Locate platelets.
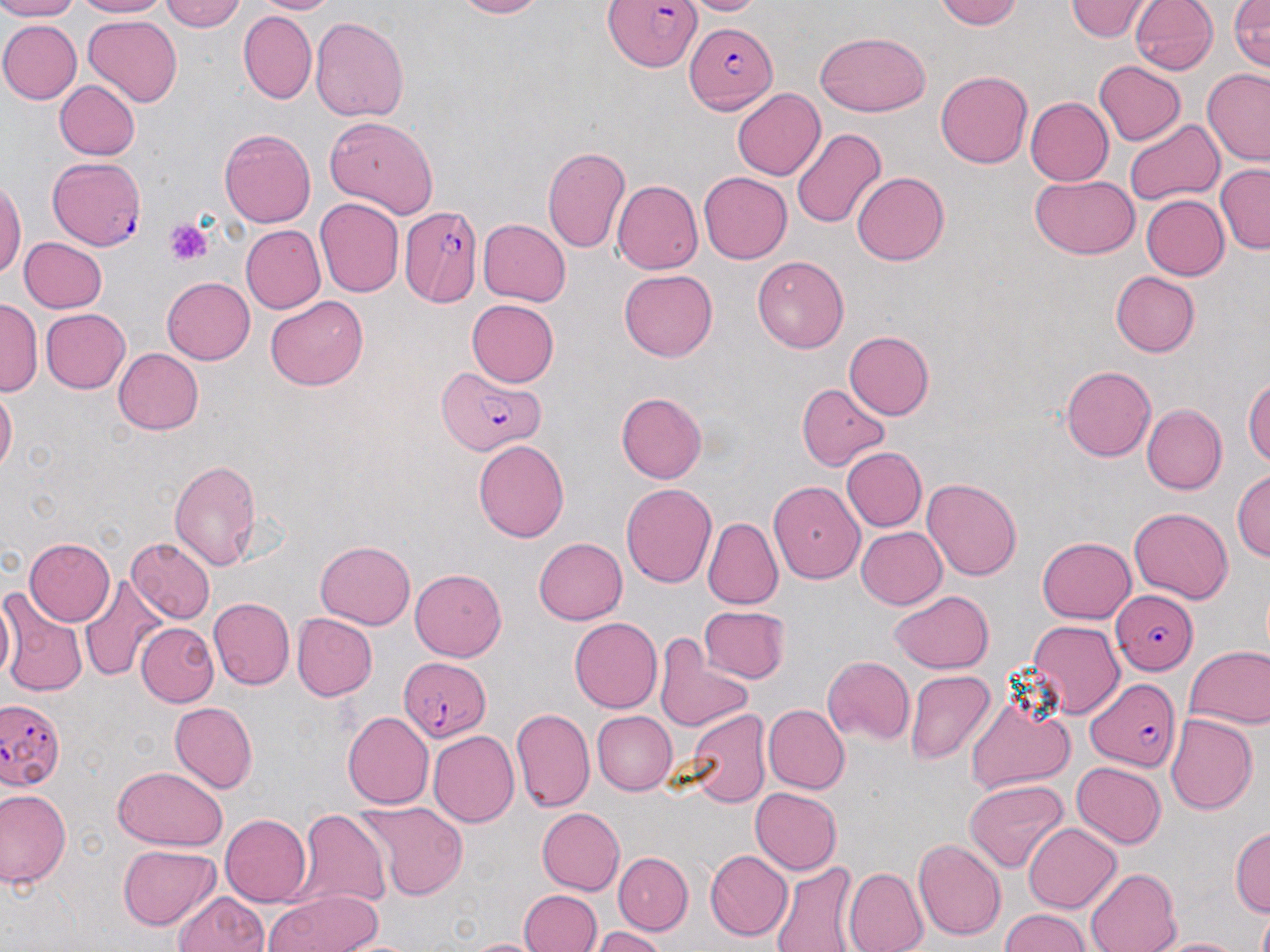
Approximate bounding boxes as named x1/y1/x2/y2 corners in pixels.
Platelets: (x1=163, y1=218, x2=214, y2=268).

Summary:
  - Plasmodium falciparum-infected red blood cell locations: (x1=600, y1=0, x2=703, y2=78), (x1=686, y1=19, x2=778, y2=111), (x1=46, y1=156, x2=148, y2=251), (x1=399, y1=204, x2=486, y2=309), (x1=434, y1=366, x2=549, y2=452), (x1=1110, y1=589, x2=1199, y2=674), (x1=398, y1=655, x2=489, y2=743), (x1=1086, y1=678, x2=1182, y2=774), (x1=0, y1=698, x2=65, y2=798)
  - Uninfected red blood cell locations: (x1=0, y1=0, x2=83, y2=22), (x1=69, y1=0, x2=174, y2=18), (x1=157, y1=0, x2=249, y2=32), (x1=254, y1=0, x2=336, y2=15), (x1=446, y1=0, x2=552, y2=18), (x1=685, y1=0, x2=761, y2=16), (x1=936, y1=0, x2=1024, y2=30), (x1=1068, y1=0, x2=1148, y2=42), (x1=1130, y1=0, x2=1217, y2=75), (x1=1230, y1=0, x2=1270, y2=70), (x1=238, y1=10, x2=317, y2=106), (x1=83, y1=15, x2=183, y2=106), (x1=310, y1=15, x2=409, y2=121), (x1=0, y1=19, x2=80, y2=105), (x1=816, y1=32, x2=930, y2=116), (x1=1093, y1=60, x2=1185, y2=146), (x1=936, y1=70, x2=1036, y2=168), (x1=1200, y1=71, x2=1270, y2=165), (x1=56, y1=78, x2=141, y2=160), (x1=733, y1=89, x2=827, y2=181), (x1=1026, y1=96, x2=1113, y2=186), (x1=325, y1=117, x2=437, y2=217), (x1=1124, y1=118, x2=1224, y2=208), (x1=219, y1=127, x2=315, y2=228), (x1=791, y1=128, x2=886, y2=230), (x1=544, y1=143, x2=632, y2=255), (x1=1215, y1=164, x2=1270, y2=254), (x1=699, y1=171, x2=792, y2=263), (x1=851, y1=172, x2=946, y2=266), (x1=1031, y1=174, x2=1139, y2=260), (x1=0, y1=177, x2=24, y2=285), (x1=613, y1=179, x2=702, y2=273), (x1=1139, y1=194, x2=1228, y2=281), (x1=314, y1=199, x2=402, y2=299), (x1=475, y1=217, x2=569, y2=308), (x1=239, y1=225, x2=324, y2=314), (x1=19, y1=236, x2=106, y2=312), (x1=753, y1=254, x2=849, y2=349), (x1=619, y1=269, x2=717, y2=361), (x1=1110, y1=271, x2=1200, y2=357), (x1=162, y1=277, x2=255, y2=363), (x1=265, y1=295, x2=368, y2=392), (x1=0, y1=299, x2=40, y2=398), (x1=467, y1=300, x2=559, y2=387), (x1=42, y1=307, x2=131, y2=393), (x1=844, y1=331, x2=936, y2=419), (x1=111, y1=346, x2=203, y2=435), (x1=1059, y1=363, x2=1156, y2=462), (x1=1244, y1=373, x2=1270, y2=474), (x1=798, y1=384, x2=893, y2=472), (x1=1, y1=388, x2=17, y2=476), (x1=616, y1=391, x2=707, y2=483), (x1=1142, y1=405, x2=1226, y2=494), (x1=472, y1=441, x2=568, y2=542), (x1=839, y1=447, x2=927, y2=532), (x1=169, y1=458, x2=262, y2=573), (x1=1233, y1=469, x2=1268, y2=568), (x1=922, y1=476, x2=1023, y2=581), (x1=620, y1=481, x2=717, y2=590), (x1=769, y1=483, x2=864, y2=582), (x1=1127, y1=503, x2=1232, y2=601), (x1=703, y1=518, x2=781, y2=611), (x1=854, y1=526, x2=945, y2=609), (x1=532, y1=536, x2=627, y2=625), (x1=1036, y1=536, x2=1136, y2=625), (x1=23, y1=537, x2=115, y2=626), (x1=125, y1=537, x2=213, y2=623), (x1=315, y1=541, x2=415, y2=629), (x1=411, y1=569, x2=505, y2=662), (x1=79, y1=574, x2=166, y2=685), (x1=0, y1=587, x2=86, y2=698), (x1=890, y1=589, x2=993, y2=672), (x1=209, y1=598, x2=294, y2=690), (x1=700, y1=605, x2=790, y2=684), (x1=294, y1=613, x2=378, y2=701), (x1=569, y1=617, x2=661, y2=713), (x1=1026, y1=619, x2=1123, y2=718), (x1=136, y1=622, x2=217, y2=706), (x1=656, y1=640, x2=753, y2=730), (x1=1183, y1=644, x2=1270, y2=731), (x1=823, y1=656, x2=914, y2=746), (x1=905, y1=671, x2=995, y2=764), (x1=964, y1=691, x2=1075, y2=798), (x1=168, y1=701, x2=256, y2=793), (x1=761, y1=705, x2=847, y2=793), (x1=681, y1=706, x2=770, y2=809), (x1=511, y1=708, x2=593, y2=812), (x1=342, y1=709, x2=434, y2=806), (x1=590, y1=710, x2=676, y2=794), (x1=1165, y1=713, x2=1259, y2=813), (x1=428, y1=730, x2=519, y2=826), (x1=1072, y1=762, x2=1166, y2=850), (x1=112, y1=766, x2=226, y2=850), (x1=965, y1=780, x2=1069, y2=874), (x1=2, y1=787, x2=71, y2=889), (x1=751, y1=788, x2=841, y2=875), (x1=354, y1=803, x2=468, y2=900), (x1=535, y1=807, x2=624, y2=895), (x1=296, y1=808, x2=389, y2=910), (x1=220, y1=812, x2=311, y2=905), (x1=1023, y1=823, x2=1121, y2=914), (x1=1231, y1=824, x2=1269, y2=916), (x1=913, y1=838, x2=1007, y2=940), (x1=118, y1=844, x2=218, y2=929), (x1=706, y1=849, x2=792, y2=940), (x1=615, y1=851, x2=692, y2=933), (x1=770, y1=861, x2=861, y2=952), (x1=843, y1=868, x2=928, y2=952), (x1=1086, y1=868, x2=1180, y2=952), (x1=264, y1=890, x2=387, y2=952), (x1=520, y1=890, x2=600, y2=952), (x1=171, y1=891, x2=270, y2=952), (x1=997, y1=908, x2=1092, y2=952), (x1=1255, y1=909, x2=1270, y2=952), (x1=590, y1=925, x2=670, y2=952), (x1=1149, y1=934, x2=1250, y2=952), (x1=462, y1=935, x2=542, y2=952)
  - Slide-level diagnosis: Plasmodium falciparum
  - Image size: 1270×952 pixels
  - Field of view: one of a larger specimen
  - Preparation: thin blood film
  - Magnification: 1000x
  - Stain: May-Grünwald-Giemsa
  - Modality: light microscopy